Locate every Babesia divergens-infected red blood cell.
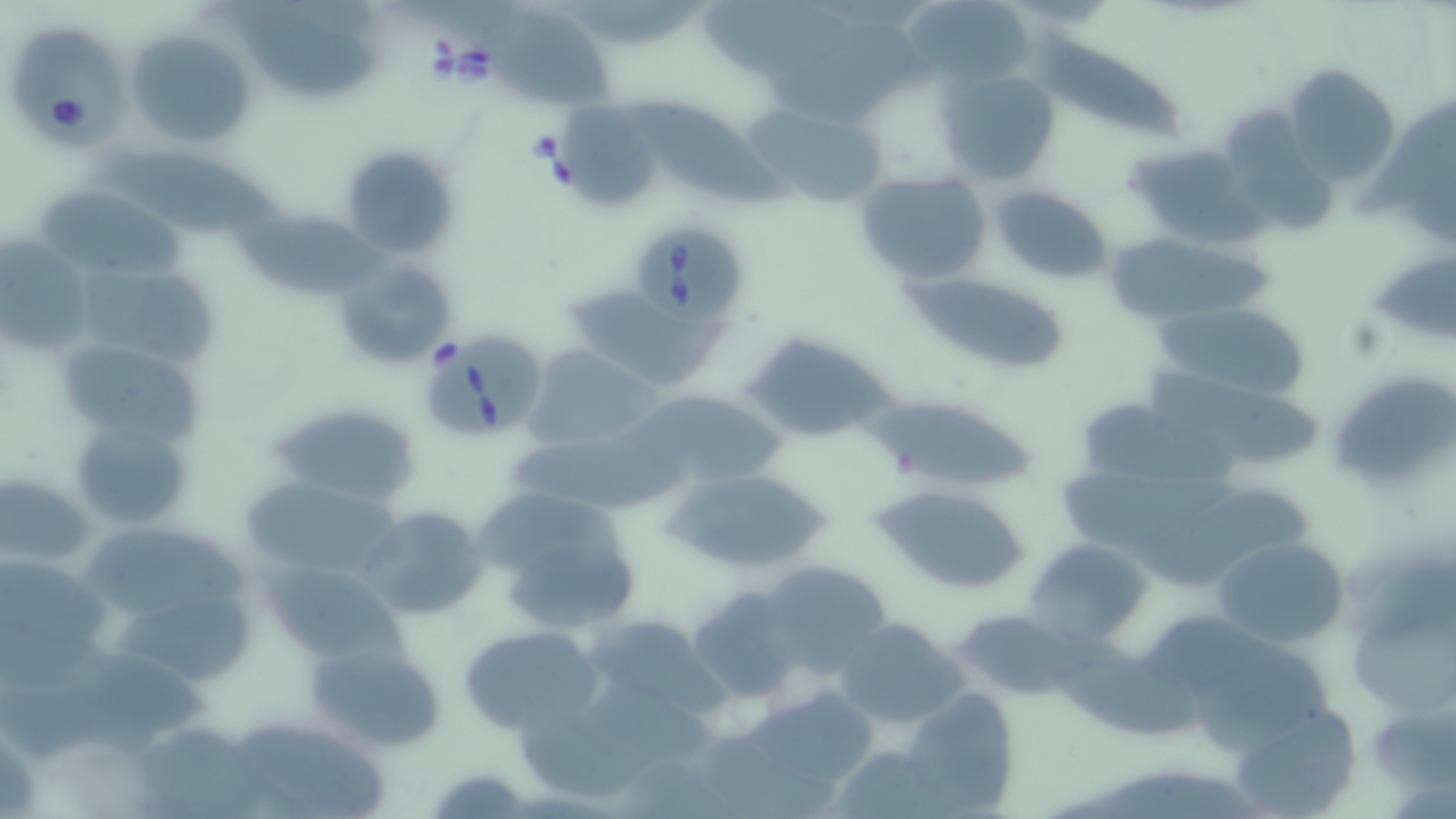
Approximate bounding boxes as [x1, y1, x2, y2] in pixels.
Babesia divergens-infected red blood cells: [8, 26, 134, 155], [629, 228, 754, 331], [430, 327, 549, 436].

slide-level diagnosis = Babesia divergens
uninfected red blood cell locations = approximate bounding boxes as [x1, y1, x2, y2] in pixels: [702, 3, 862, 82], [905, 5, 1036, 85], [481, 8, 615, 106], [237, 14, 386, 99], [125, 29, 259, 148], [1037, 34, 1184, 139], [1280, 64, 1400, 187], [938, 67, 1063, 189], [623, 96, 793, 214], [747, 102, 891, 212], [1359, 104, 1456, 215], [564, 110, 665, 213], [1223, 111, 1339, 234], [1122, 142, 1258, 248], [337, 143, 459, 258], [102, 148, 285, 234], [854, 170, 993, 288], [987, 183, 1115, 285], [39, 187, 186, 283], [231, 209, 387, 300], [1102, 232, 1279, 328], [0, 235, 91, 349], [1375, 252, 1456, 347], [329, 255, 455, 372], [75, 264, 216, 363], [903, 276, 1066, 375], [567, 289, 728, 387], [1150, 300, 1313, 404], [740, 339, 899, 438], [60, 345, 205, 439], [521, 345, 661, 451], [1333, 381, 1456, 485], [621, 388, 788, 497], [868, 395, 1037, 494], [1084, 400, 1247, 488], [271, 402, 420, 506], [71, 412, 195, 531], [506, 428, 689, 507], [1064, 464, 1240, 541], [666, 468, 836, 577], [0, 473, 96, 568], [242, 476, 397, 579], [876, 483, 1033, 595], [471, 495, 642, 576], [362, 505, 489, 623], [85, 523, 256, 620], [1210, 536, 1351, 651], [1025, 539, 1149, 645], [505, 541, 639, 625], [758, 559, 894, 675], [255, 561, 409, 668], [684, 585, 803, 700], [119, 590, 258, 685], [1357, 602, 1456, 708], [953, 608, 1082, 701], [1133, 616, 1292, 687], [832, 618, 966, 728], [460, 624, 603, 733], [306, 640, 450, 754], [1200, 650, 1334, 750], [735, 684, 880, 798], [901, 686, 1024, 813], [1368, 700, 1453, 799], [1228, 704, 1360, 816], [241, 724, 388, 813], [426, 764, 529, 817]
field of view = one of a larger specimen
modality = light microscopy
preparation = thin blood smear
magnification = 1000x
stain = May-Grünwald-Giemsa
image size = 1456×819 pixels